Classify this cell by malaria status.
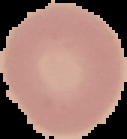

It is uninfected.

Summary:
  - Image size: 127×139 pixels
  - Image type: segmented cell region on a black background
  - Preparation: thin blood film